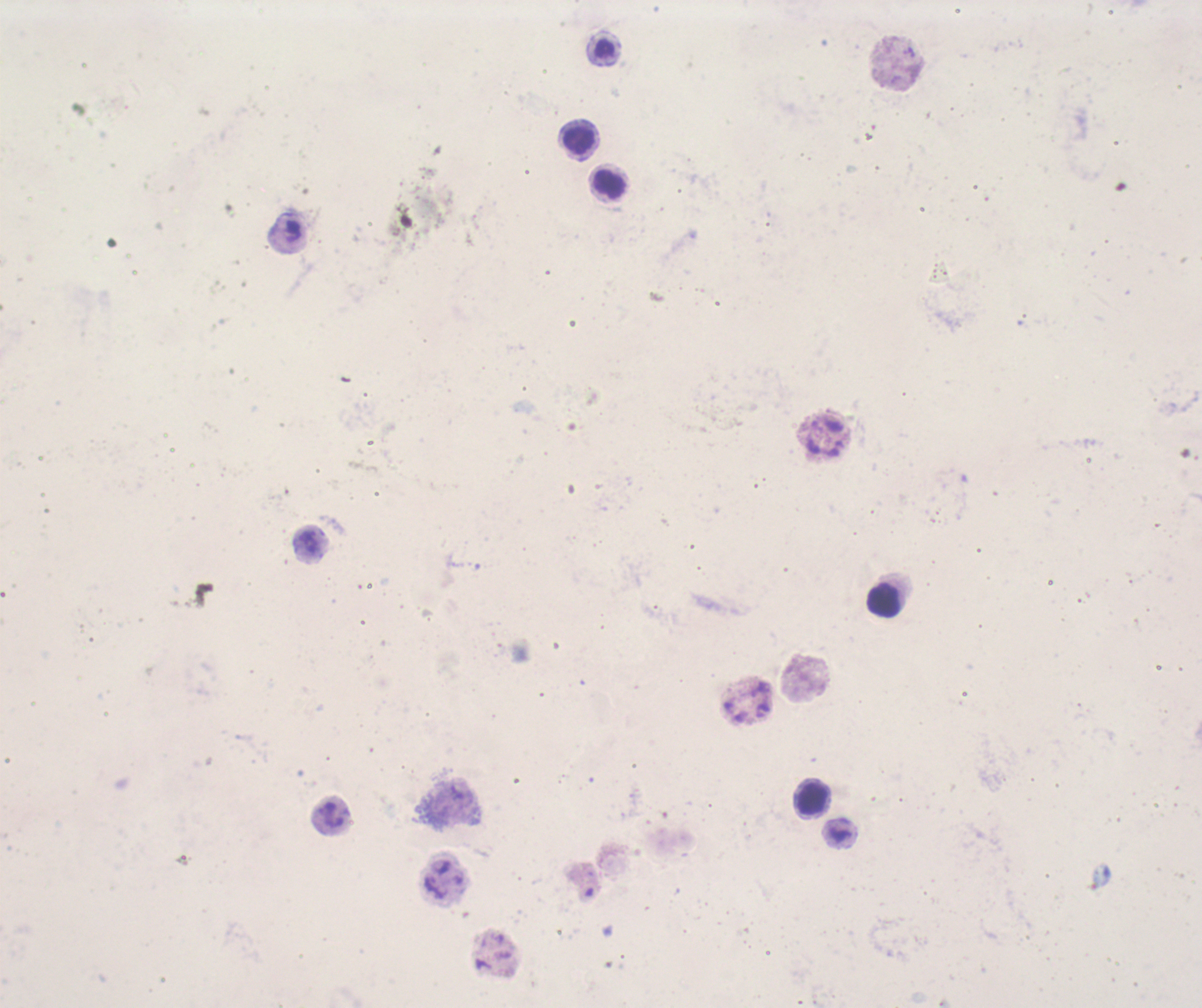

Approximate centers as [x, y] in pixels. Leukocyte locations: [605, 48], [579, 142], [610, 185], [884, 599], [812, 799]. Coloration quality: bad. Romanowsky stain. Single field of view. Captured at 100x magnification. Result: no malaria parasites detected. Image is 1202×1008 pixels. Thick blood smear. Previously used in a real diagnosis. Background quality: poor.